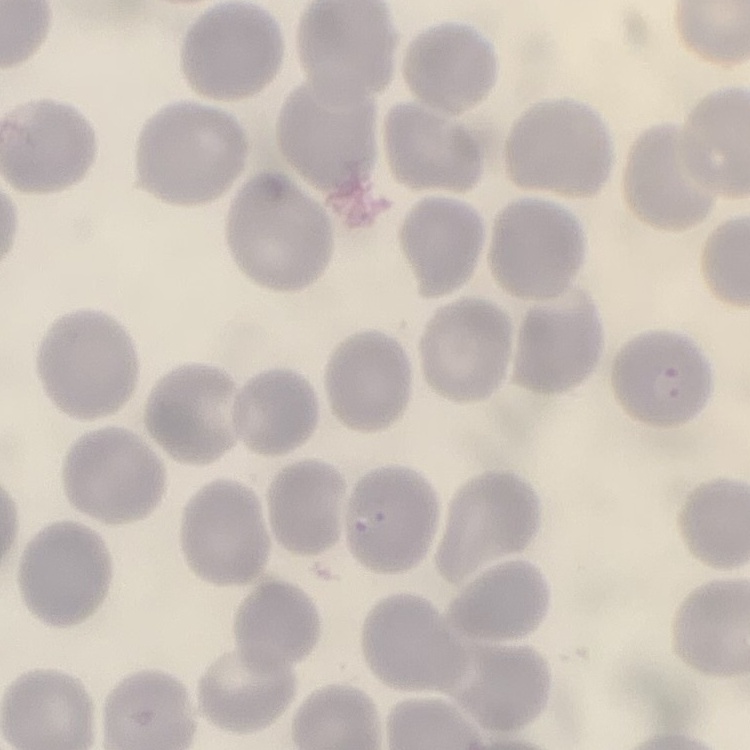
The erythrocytes exhibit no rouleaux formation. One tile cut from a larger photomicrograph. Stained with either Field's or Giemsa. Thin blood smear.